Point out each Plasmodium parasite.
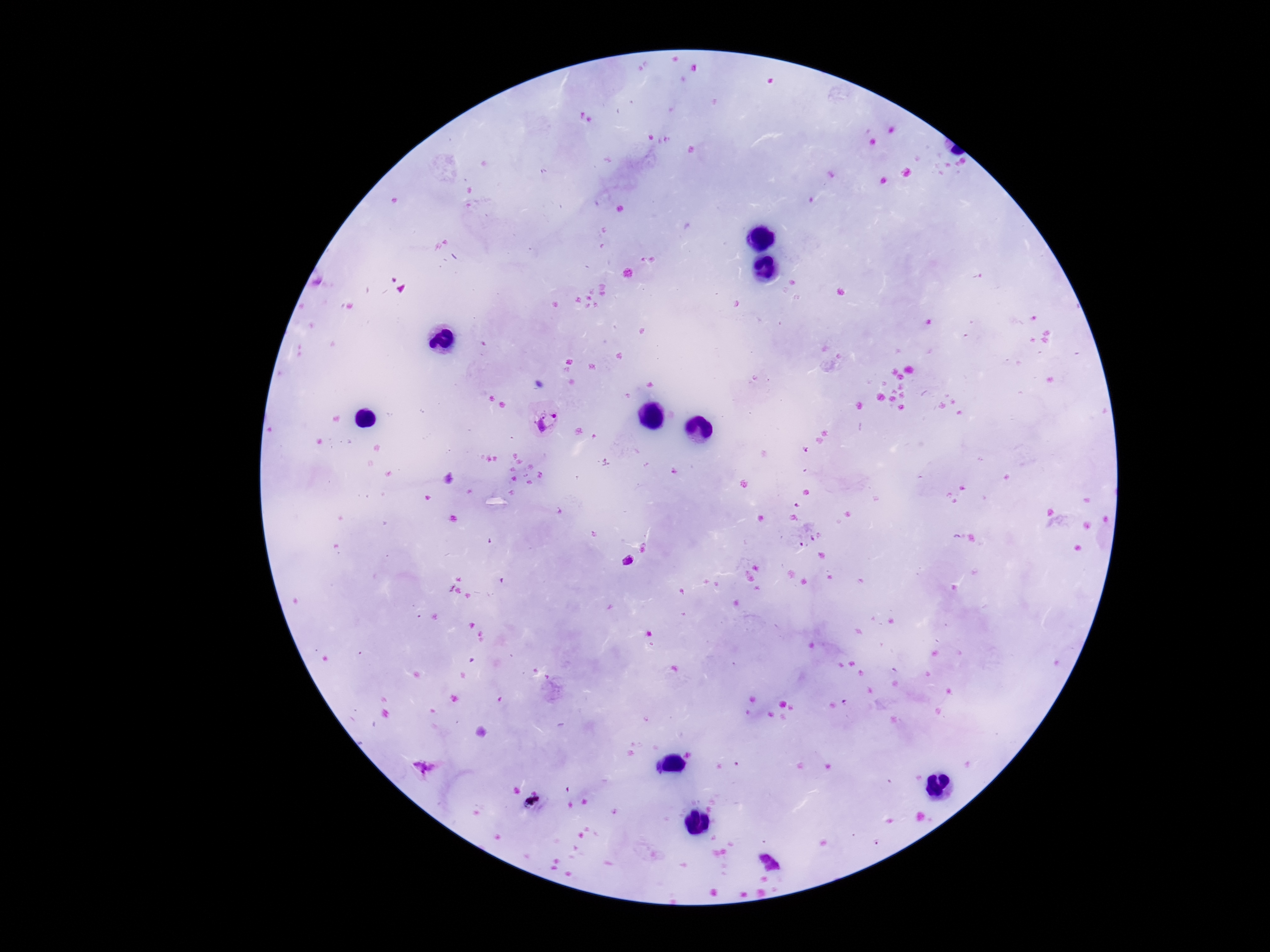

Approximate object centers, in pixels from the top-left corner.
Plasmodium parasites: (x=547, y=420), (x=629, y=561), (x=769, y=862).

Thick blood smear. 100x magnification. Patient malaria status: positive. Giemsa-stained preparation. Photographed through the microscope eyepiece with a smartphone camera. Single field of view. Image is 1270×952 pixels.